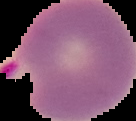

result = malaria parasites identified
preparation = thin blood smear
image type = cell region segmented out of the field of view; surrounding area masked to black
image size = 136×121 pixels